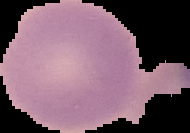

Summary:
  - Image type: cell region segmented out of the field of view; surrounding area masked to black
  - Result: no malaria parasites detected
  - Image size: 190×133 pixels
  - Preparation: thin blood film